Point out Plasmodium parasites and leukocytes.
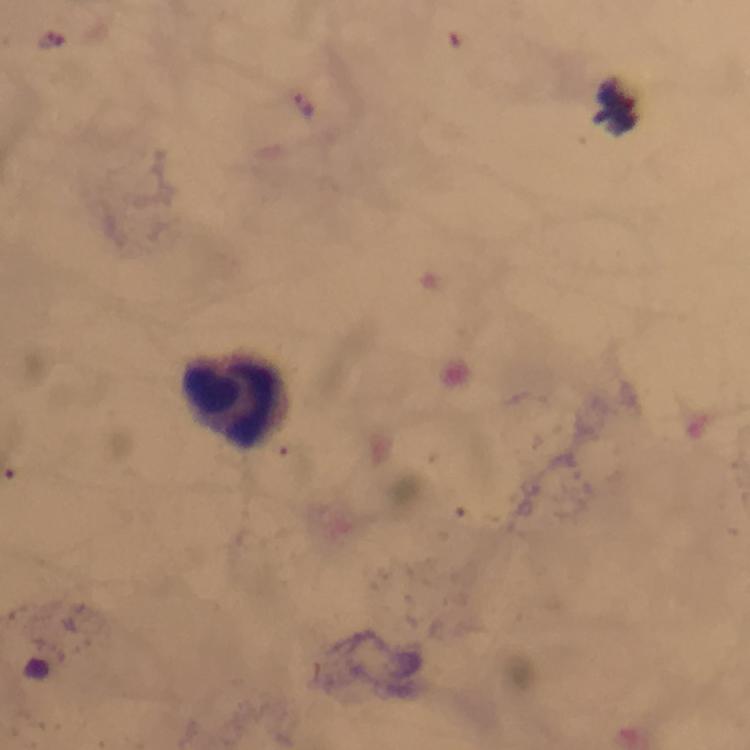
Approximate centers as (x, y) in pixels.
Plasmodium parasites: (304, 105).
Leukocytes: (234, 399).

Immersion oil was used. Giemsa-stained preparation. 100x magnification. Image is 750×750 pixels. A crop from one field of view. From a malaria diagnostic workup. Smartphone photograph taken through a microscope. Thick smear.